Locate every blood parasite and identify its species.
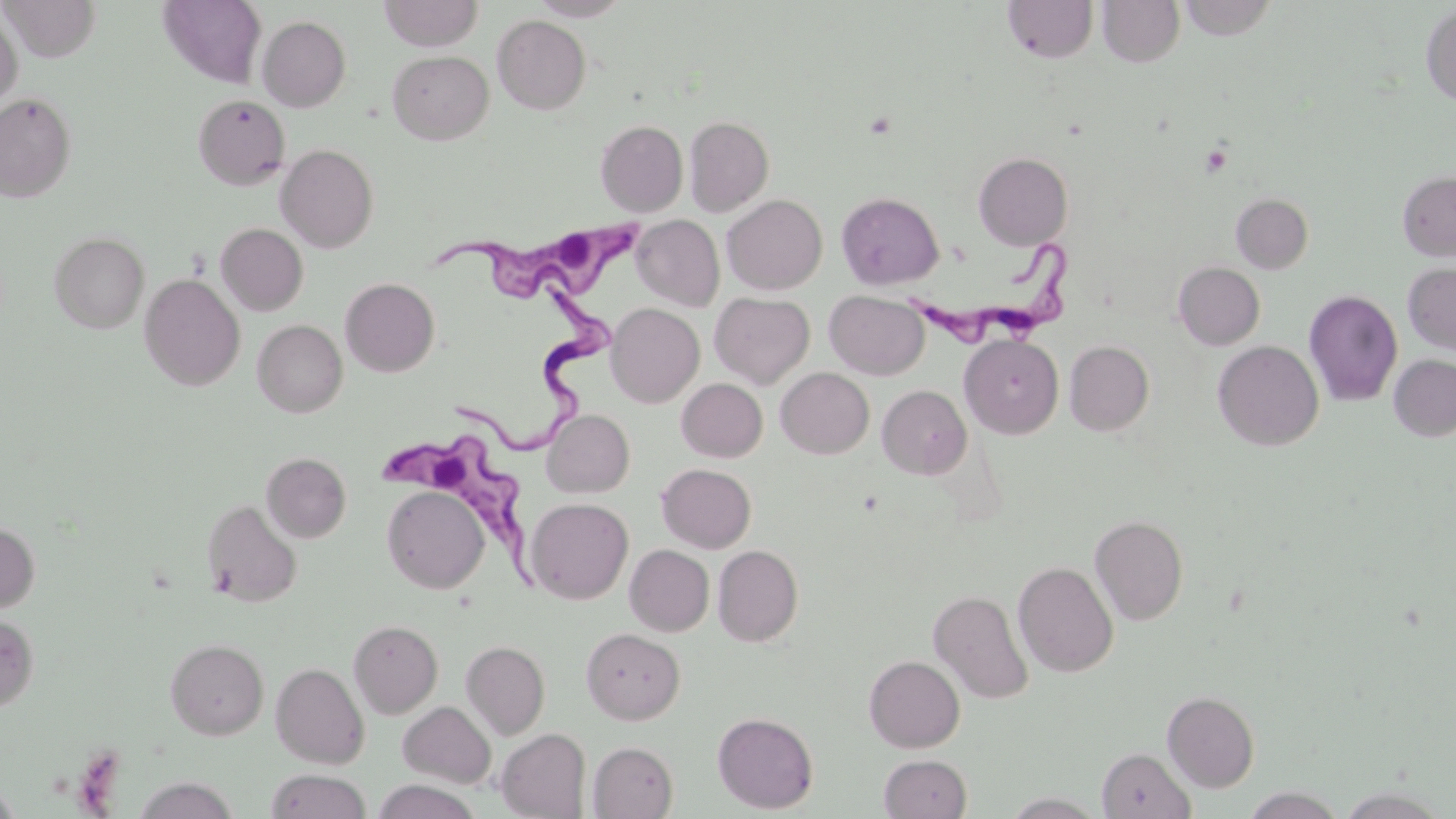

Approximate bounding boxes as (x1, y1, x2, y2) in pixels.
Trypanosoma brucei: (437, 218, 657, 301), (904, 243, 1072, 355), (460, 274, 631, 447), (367, 434, 538, 599).
No Plasmodium falciparum, Plasmodium ovale, Plasmodium malariae, Plasmodium vivax, or Babesia divergens observed.

Summary:
  - Platelet locations: (1199, 143, 1232, 177)
  - Uninfected red blood cell locations: (2, 0, 101, 62), (378, 0, 484, 50), (529, 0, 632, 20), (1003, 0, 1099, 62), (1096, 0, 1185, 67), (1177, 0, 1279, 41), (157, 1, 267, 87), (1421, 4, 1456, 106), (0, 10, 23, 113), (493, 15, 591, 115), (257, 16, 351, 112), (387, 50, 494, 144), (0, 93, 76, 201), (193, 94, 290, 190), (684, 116, 774, 216), (595, 120, 689, 217), (276, 144, 378, 253), (973, 152, 1073, 249), (1397, 171, 1456, 261), (836, 192, 944, 289), (1231, 193, 1313, 274), (722, 194, 827, 294), (632, 215, 724, 310), (216, 223, 308, 316), (50, 231, 149, 333), (1173, 262, 1265, 350), (1402, 262, 1456, 355), (140, 274, 245, 391), (340, 278, 440, 376), (1304, 289, 1403, 406), (824, 290, 929, 379), (710, 292, 814, 389), (606, 303, 704, 407), (253, 319, 347, 417), (960, 334, 1064, 438), (1064, 340, 1155, 436), (1213, 340, 1324, 450), (1388, 354, 1456, 442), (776, 367, 874, 458), (677, 378, 767, 462), (877, 385, 972, 479), (542, 409, 634, 498), (261, 452, 351, 542), (657, 463, 756, 553), (381, 486, 490, 593), (526, 498, 633, 603), (202, 499, 302, 607), (1090, 515, 1188, 625), (0, 521, 40, 613), (713, 544, 804, 646), (625, 545, 714, 635), (1013, 561, 1118, 677), (929, 589, 1033, 703), (0, 612, 39, 712), (348, 620, 443, 718), (581, 626, 685, 724), (165, 638, 268, 739), (461, 640, 550, 739), (864, 655, 965, 752), (271, 662, 370, 768), (1162, 690, 1259, 792), (398, 702, 496, 787), (713, 711, 818, 813), (496, 729, 591, 819), (589, 741, 678, 818), (1097, 748, 1195, 819), (879, 754, 971, 818), (266, 770, 372, 819), (132, 776, 239, 818), (372, 779, 483, 819), (0, 782, 21, 819), (1331, 785, 1453, 818), (1240, 787, 1347, 818)
  - Slide-level diagnosis: Trypanosoma brucei
  - Magnification: 1000x
  - Preparation: thin blood film
  - Stain: May-Grünwald-Giemsa
  - Image size: 1456×819 pixels
  - Modality: light microscopy
  - Field of view: single